Comment on the morphology of the erythrocytes.
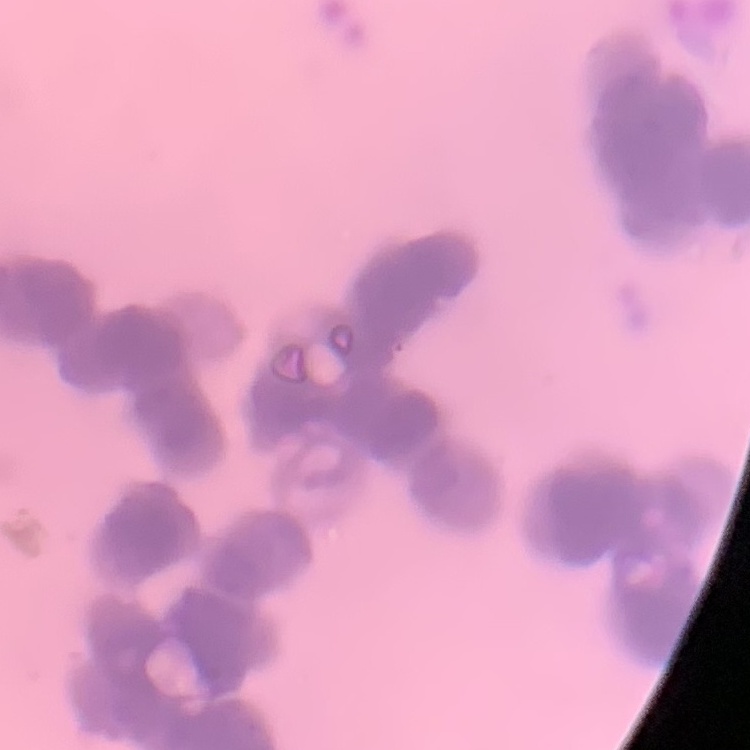

Rouleaux formation.

Square crop of a larger photomicrograph. Field's or Giemsa stain. Thin blood film.